Assess this cell for malaria.
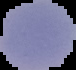
Parasitized.

Summary:
  - Image type: segmented cell region with the area outside set to black
  - Preparation: thin blood smear
  - Image size: 76×70 pixels